Report the malaria status of this cell.
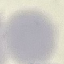

It is uninfected.

preparation: thin blood film
image_type: automatically extracted cell patch, resized to 64 × 64 pixels
capture: smartphone camera at the microscope eyepiece
stain: Giemsa